Identify the blood parasite species.
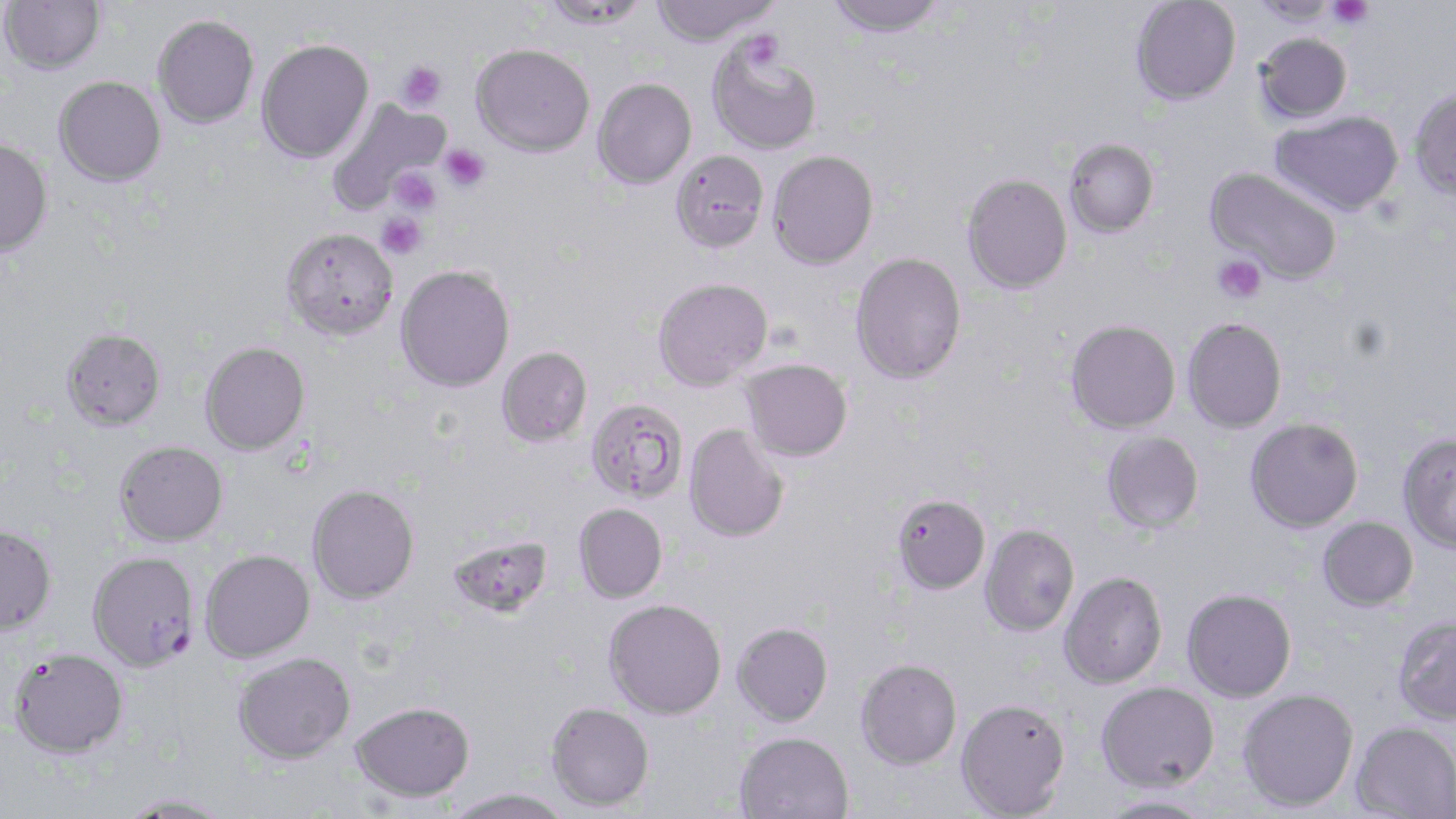
Plasmodium falciparum.

Approximate bounding boxes as [x1, y1, x2, y2] in pixels. Plasmodium falciparum-infected red blood cell locations: [87, 551, 200, 672]. Platelet locations: [1326, 0, 1374, 29], [743, 31, 784, 70], [396, 61, 447, 112], [438, 144, 490, 192], [388, 166, 442, 217], [377, 212, 427, 260], [1213, 254, 1266, 304]. Uninfected red blood cell locations: [1, 0, 105, 74], [539, 0, 652, 30], [649, 0, 778, 46], [824, 0, 949, 37], [1130, 0, 1241, 105], [1249, 1, 1340, 26], [152, 14, 259, 127], [1255, 33, 1352, 123], [256, 38, 374, 163], [707, 41, 822, 155], [471, 43, 595, 156], [53, 76, 166, 187], [592, 77, 696, 189], [1409, 88, 1456, 200], [326, 97, 449, 215], [1269, 111, 1403, 216], [0, 138, 53, 257], [1063, 138, 1159, 238], [669, 149, 769, 253], [767, 150, 879, 270], [1204, 166, 1344, 285], [961, 173, 1073, 294], [282, 227, 398, 340], [850, 252, 967, 384], [395, 265, 515, 392], [652, 277, 773, 391], [1182, 318, 1287, 433], [1065, 319, 1180, 434], [61, 327, 167, 431], [200, 342, 310, 455], [497, 346, 593, 446], [740, 359, 853, 462], [585, 398, 688, 503], [1245, 417, 1363, 532], [684, 423, 790, 543], [1101, 431, 1204, 534], [1397, 433, 1456, 554], [114, 440, 228, 546], [307, 483, 419, 604], [890, 492, 990, 594], [573, 503, 668, 603], [1317, 516, 1419, 611], [0, 523, 57, 636], [979, 524, 1080, 636], [446, 533, 554, 619], [200, 549, 315, 662], [1059, 571, 1168, 689], [1181, 588, 1297, 702], [603, 598, 727, 719], [1392, 615, 1456, 726], [732, 622, 833, 726], [10, 649, 129, 758], [232, 652, 355, 764], [856, 658, 962, 769], [1096, 681, 1220, 792], [1237, 688, 1359, 811], [956, 698, 1071, 817], [351, 701, 474, 802], [546, 702, 654, 811], [1351, 720, 1456, 819], [735, 731, 853, 819], [443, 788, 574, 819], [1097, 793, 1218, 819], [118, 794, 235, 818]. May-Grünwald-Giemsa stain. Single field of view. Optical microscopy. 1000x magnification. Thin blood film. Image is 1456×819 pixels.